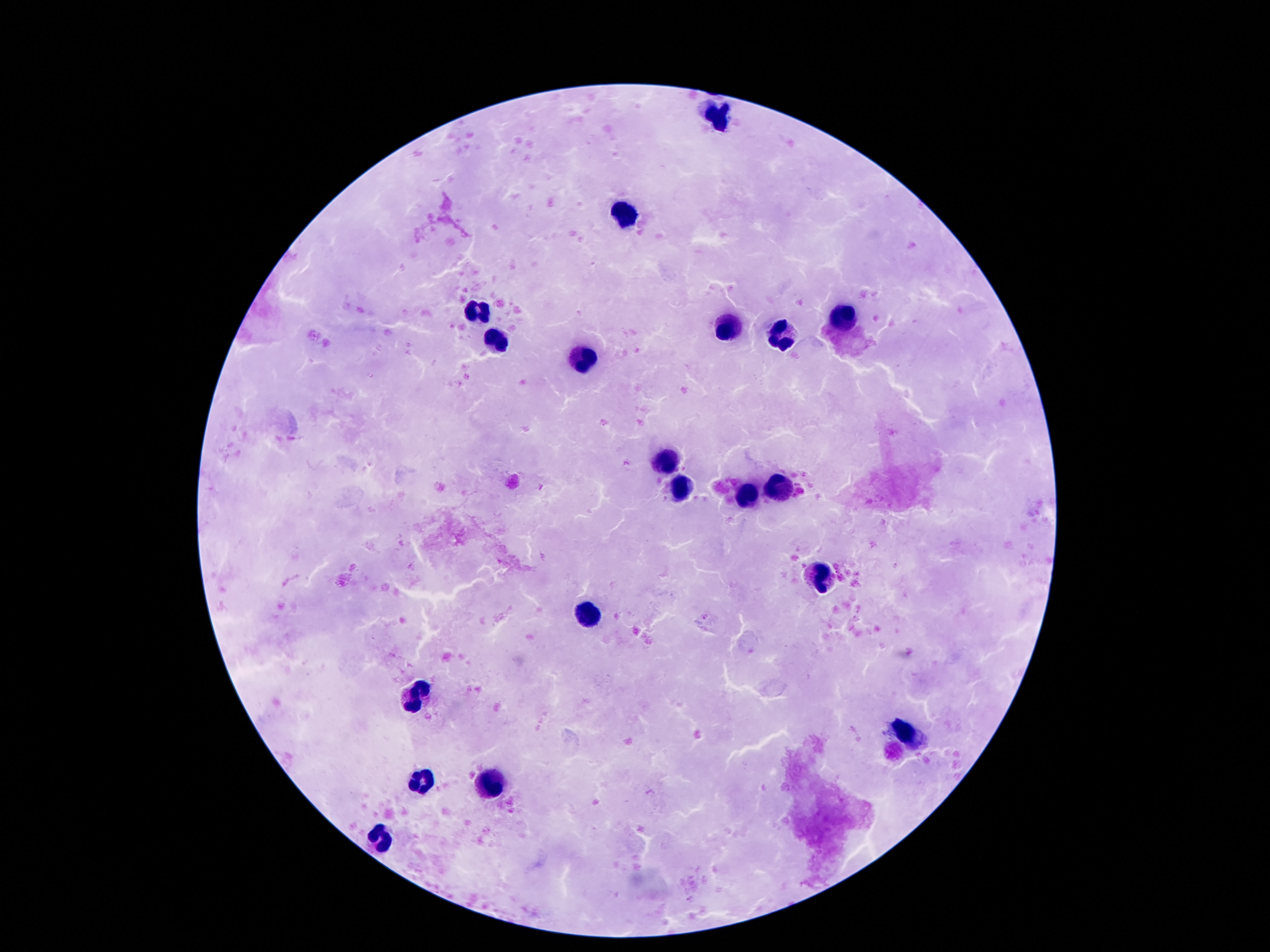 Approximate centers as (x, y) in pixels. Leukocyte locations: (718, 117), (627, 214), (479, 311), (843, 319), (729, 331), (782, 336), (498, 340), (580, 360), (668, 463), (776, 487), (681, 489), (748, 494), (821, 579), (591, 613), (416, 698), (907, 737), (418, 783), (490, 787), (378, 841). Giemsa stain. Patient malaria status: uninfected. Image is 1270×952 pixels. Thick blood smear. Smartphone photograph taken through the microscope eyepiece. 100x magnification. Single field of view.